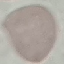
result = no malaria parasites seen
capture = smartphone camera at the microscope eyepiece
image type = cell patch, automatically extracted from a larger field of view and resized to 64 × 64 pixels
stain = Giemsa
preparation = thin blood film